Comment on the morphology of the red blood cells.
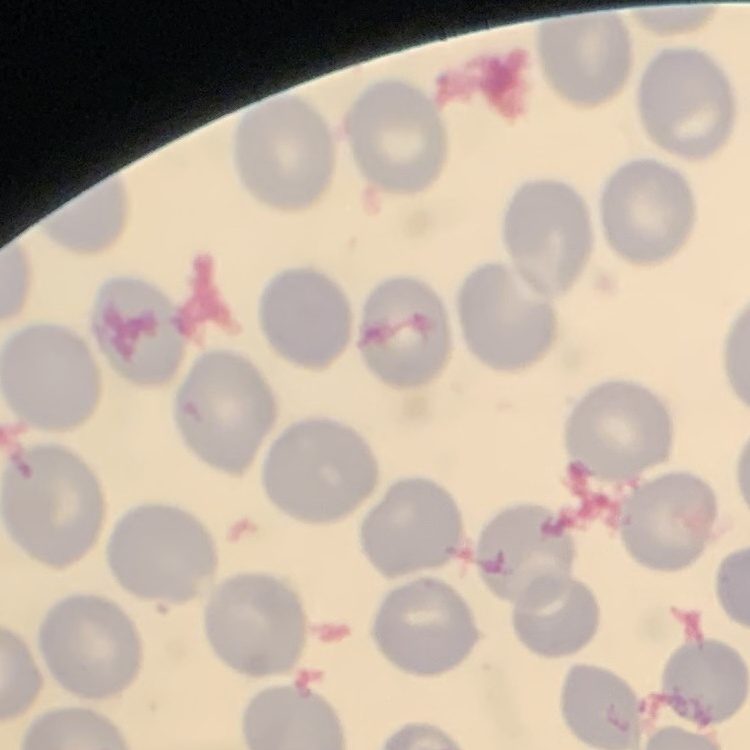
No rouleaux formation.

Summary:
  - Stain: Field's or Giemsa
  - Image type: square crop of a larger photomicrograph
  - Preparation: thin blood film